Assess this cell for malaria.
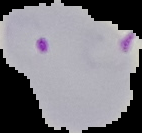
Parasitized.

image_type: cell region segmented out of the field of view; surrounding area masked to black
preparation: thin blood film
image_size: 142×133 pixels